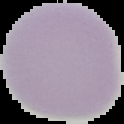

preparation: thin blood smear
malaria_status: uninfected
image_type: segmented cell region on a black background
image_size: 124×124 pixels